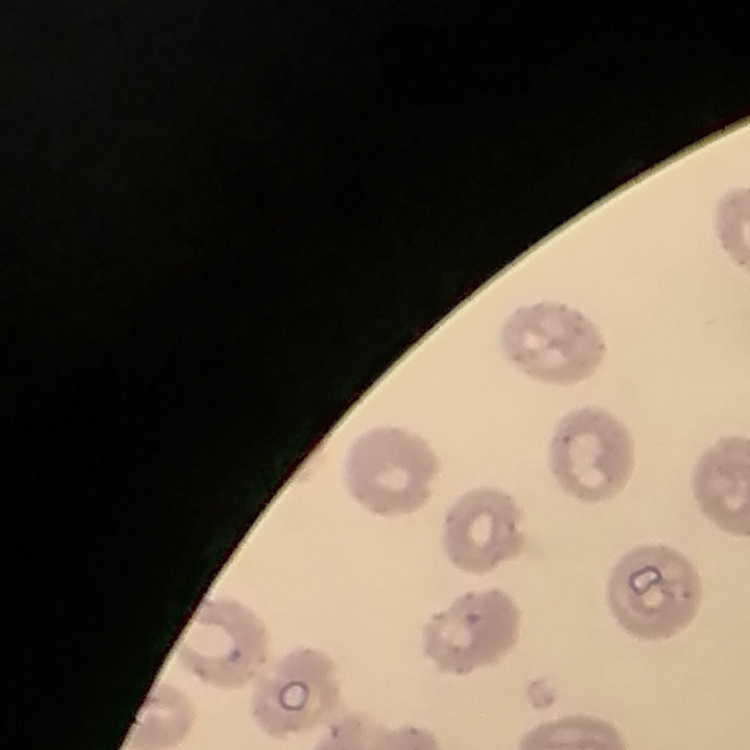

erythrocyte morphology = no rouleaux formation
stain = Field's or Giemsa
image type = one tile cut from a larger photomicrograph
preparation = thin blood smear